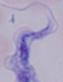 Micrograph. Captured at 1000x magnification. A trypanosome is shown.